Assess for malaria.
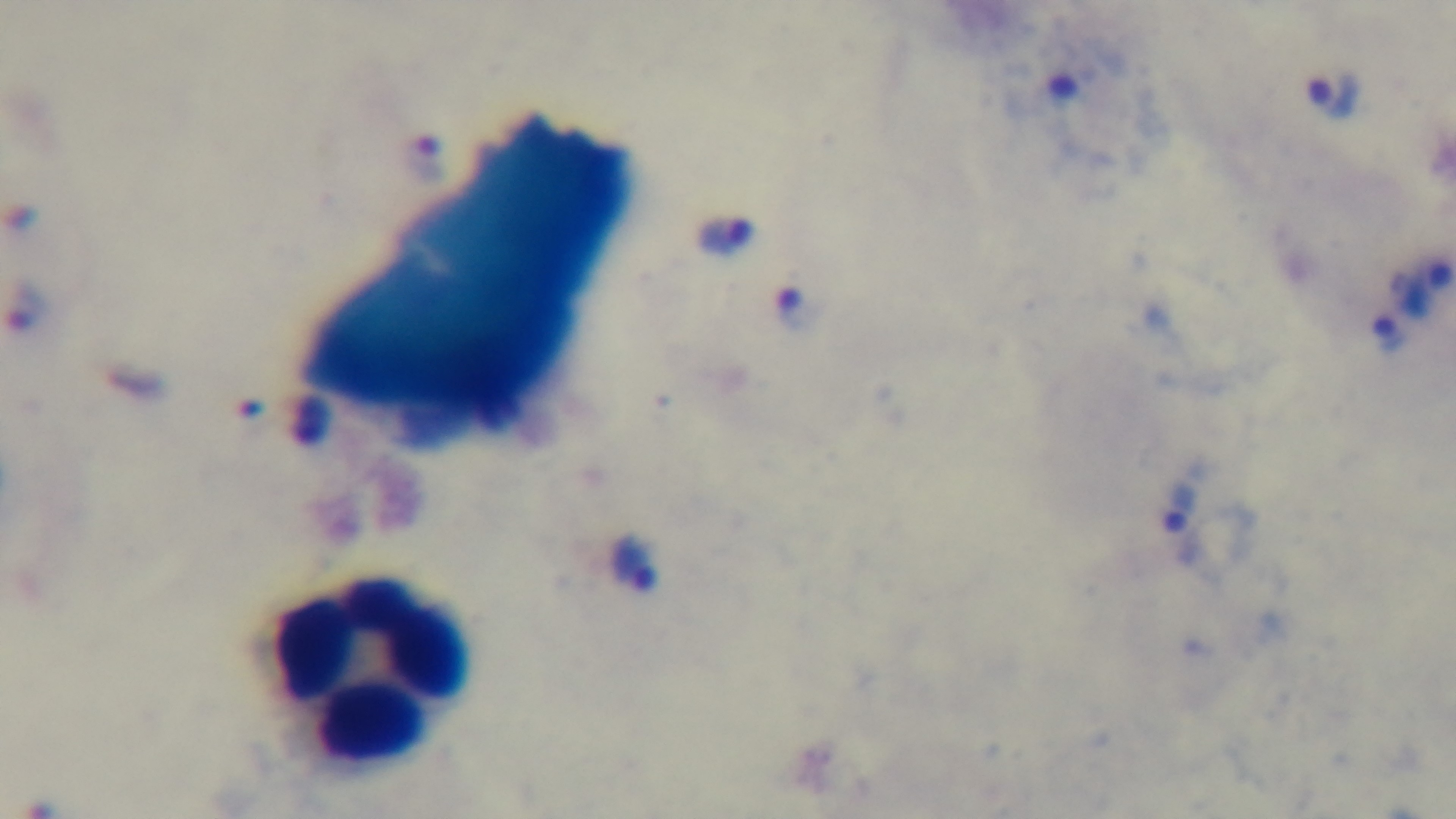

Positive.

Single field of view. Light microscopy. Giemsa-stained. Oil-immersion objective, 100x. Mounted 4K digital camera. Preparation: thick blood film.